Locate every malaria parasite and identify its life-cycle stage.
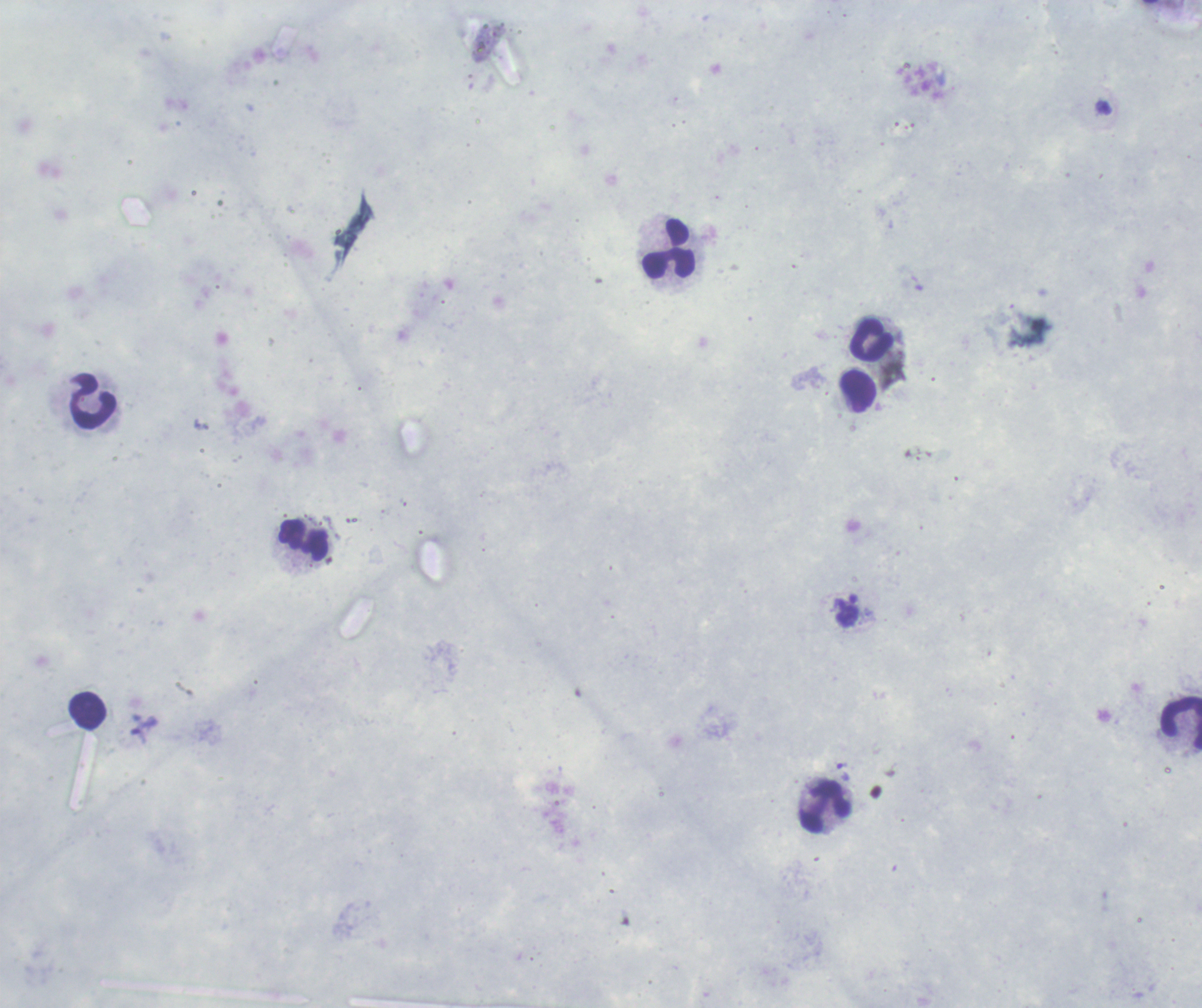

Approximate object centers, in pixels from the top-left corner.
Trophozoites: (x=843, y=771).
No schizont or gametocyte forms observed.

Approximate object centers, in pixels from the top-left corner. Leukocyte locations: (x=669, y=250), (x=872, y=341), (x=858, y=392), (x=93, y=402), (x=303, y=540), (x=87, y=711), (x=1181, y=723), (x=825, y=809). Previously used in an actual diagnosis. Background quality: unsatisfactory. Image is 1202×1008 pixels. One field from this slide. Thick smear of blood. 100x magnification. Romanowsky-stained preparation.